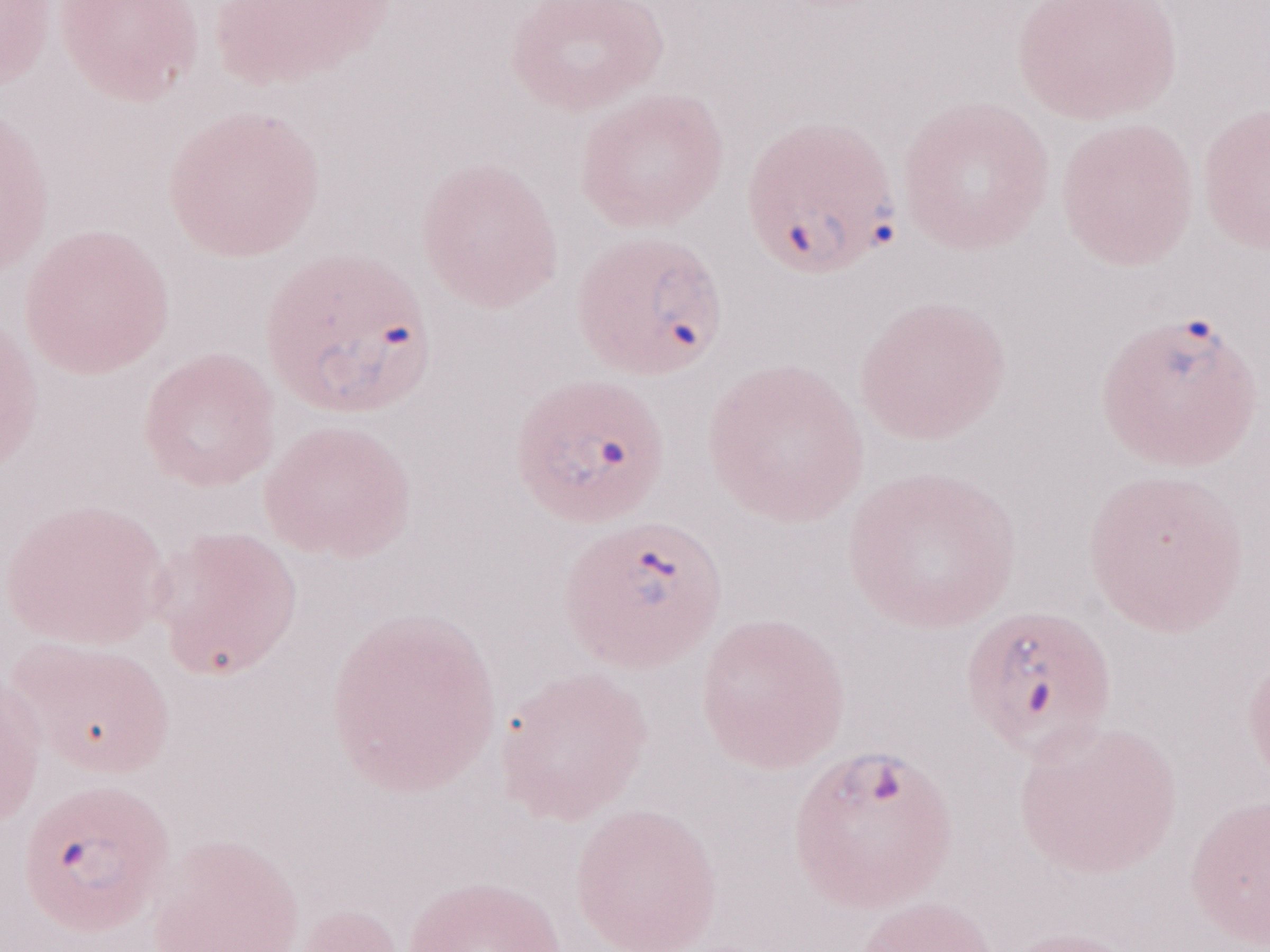

1,000x magnification. Olympus BX43 microscope, Olympus DP73 camera. Single field of view. May-Grünwald-Giemsa (MGG) stain. Image is 1270×952 pixels. Thin blood smear. Malaria diagnosis (patient-level): positive.